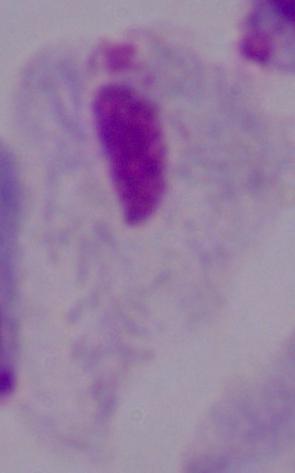

A trichomonad is seen. 1000x magnification. Photomicrograph.